Identify the parasite.
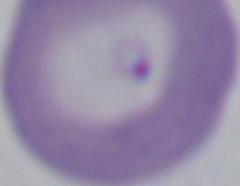

This is Babesia.

{
  "modality": "micrograph",
  "magnification": "1000x"
}